Assess the morphology of the red blood cells.
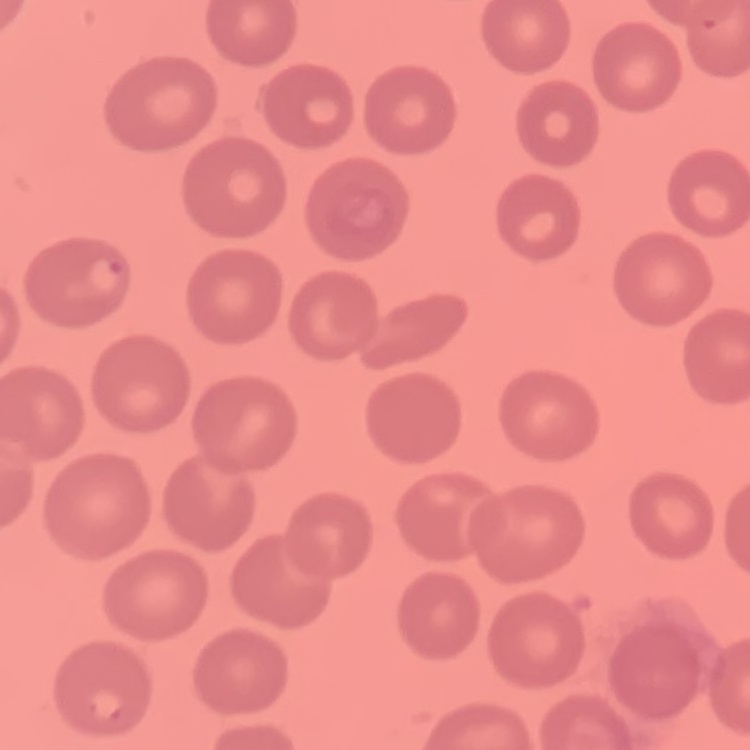

They show no rouleaux formation.

stain = Field's or Giemsa
image type = one tile cut from a larger photomicrograph
preparation = thin blood film